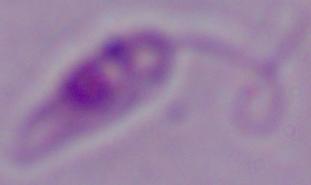
Summary:
  - Magnification: 1000x
  - Identification: Leishmania
  - Modality: micrograph